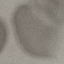
Summary:
  - Malaria status: uninfected
  - Image type: cell patch, automatically extracted from a larger field of view and resized to 64 × 64 pixels
  - Preparation: thin blood film
  - Stain: Giemsa
  - Capture: smartphone camera at the microscope eyepiece